Look for Plasmodium parasites.
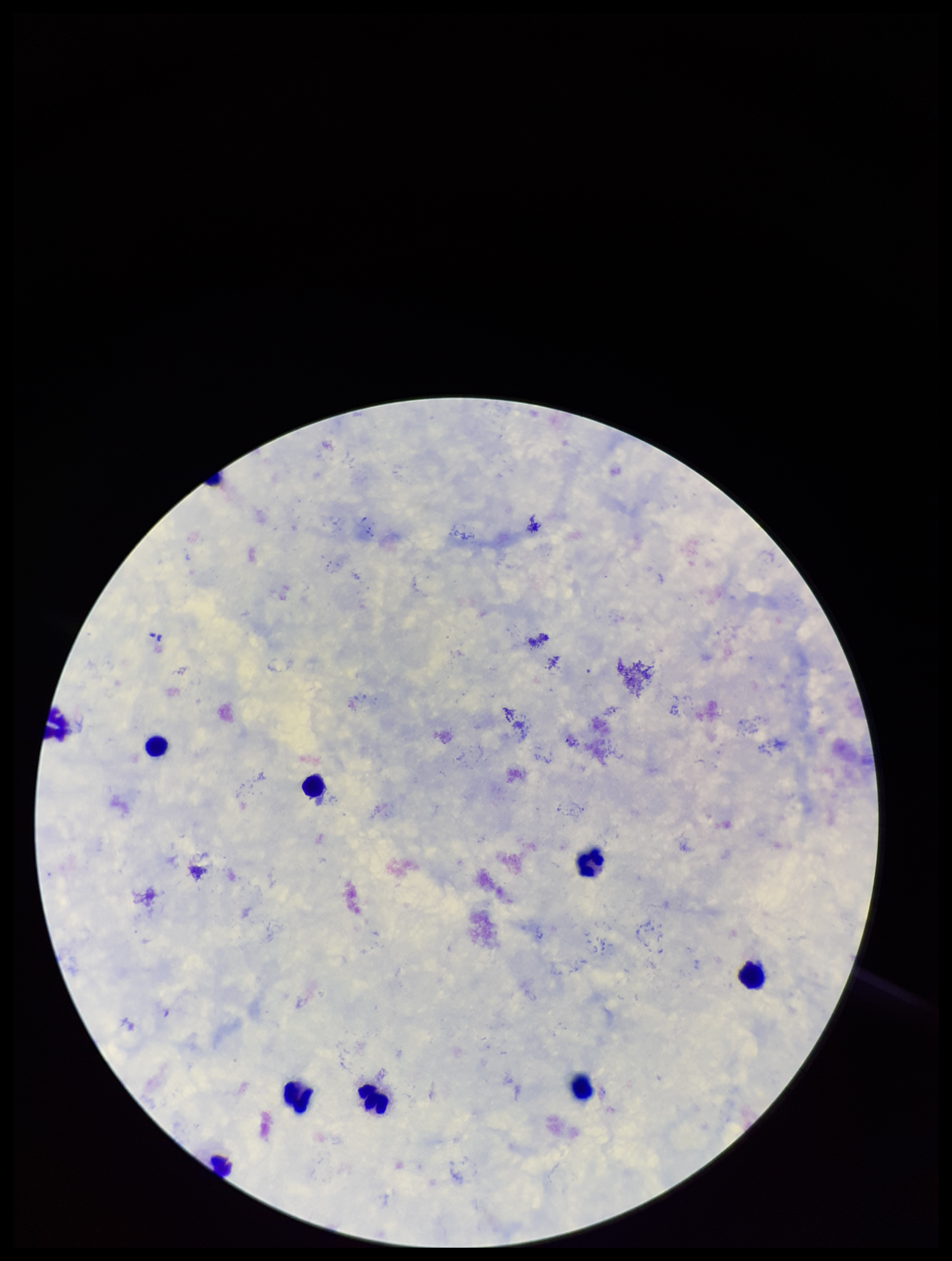

None detected.

One field from this slide. Smartphone photograph taken through the eyepiece of a microscope. Patient malaria status: negative. Parasite count: 0. Leukocyte count: 9. Image is 952×1261 pixels. Giemsa stain. Preparation: thick blood smear.